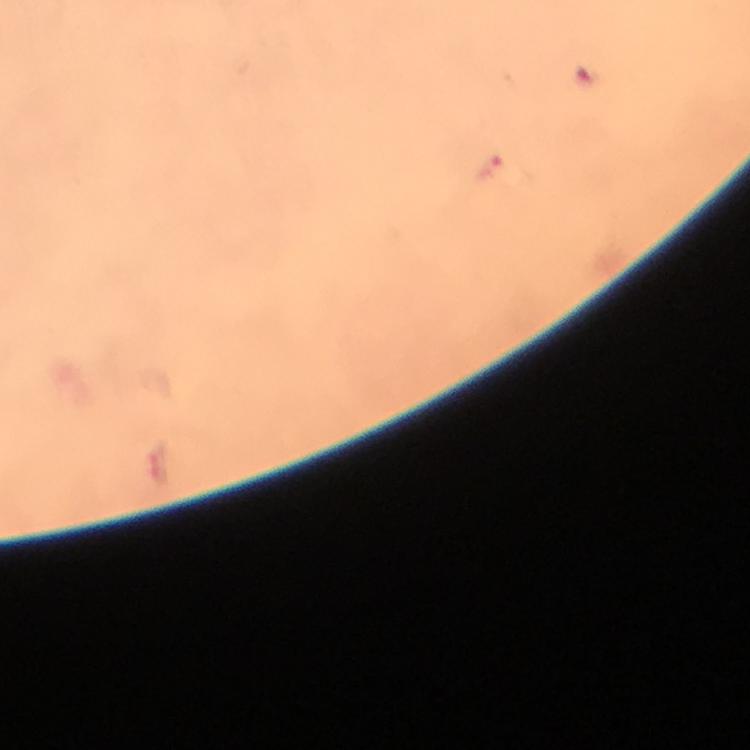

Approximate centers as (x, y) in pixels.
Summary:
  - Plasmodium parasite locations: (490, 165)
  - Magnification: 100x
  - Cropped from: one field of view
  - Context: from a malaria diagnostic workup
  - Immersion oil: used
  - Capture: smartphone mounted on the microscope
  - Preparation: thick smear
  - Image size: 750×750 pixels
  - Stain: Giemsa